Report the malaria status of this cell.
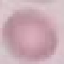

It is uninfected.

Summary:
  - Stain: Giemsa
  - Image type: automatically extracted cell patch, resized to 64 × 64 pixels
  - Preparation: thin smear
  - Capture: smartphone camera at the microscope eyepiece